Outline platelets.
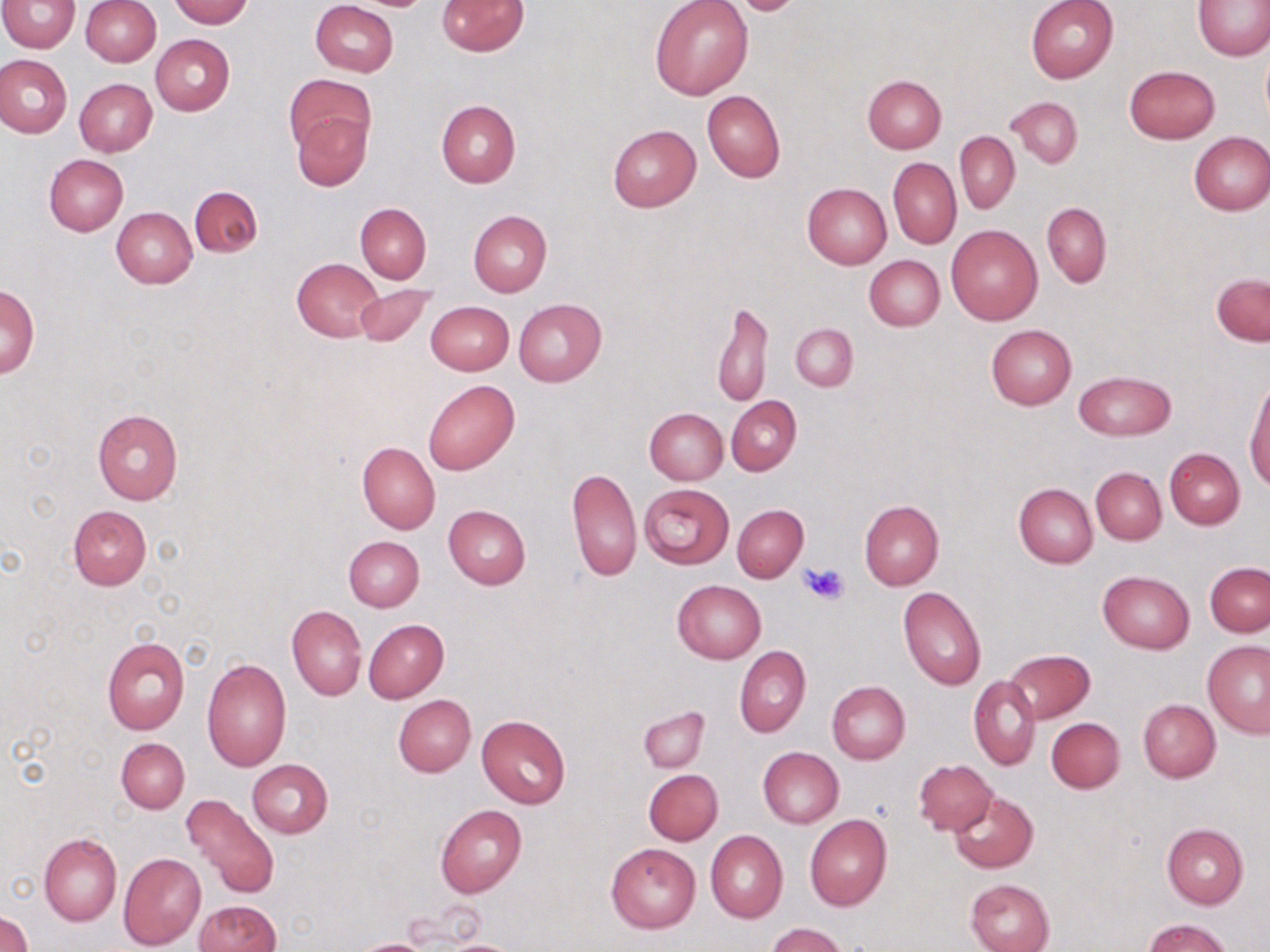

Approximate bounding boxes as [x1, y1, x2, y2] in pixels.
Platelets: [800, 561, 851, 605].

Summary:
  - Uninfected red blood cell locations: [168, 0, 252, 27], [310, 0, 399, 77], [721, 0, 807, 14], [1026, 0, 1120, 84], [1195, 0, 1270, 61], [1, 1, 80, 52], [81, 1, 161, 65], [437, 1, 528, 56], [649, 1, 753, 100], [151, 35, 235, 116], [1260, 44, 1270, 126], [0, 54, 72, 139], [1124, 65, 1219, 144], [285, 73, 375, 155], [862, 76, 947, 153], [74, 78, 157, 156], [701, 90, 785, 183], [1007, 96, 1084, 169], [436, 100, 520, 187], [293, 110, 371, 190], [607, 124, 701, 212], [955, 132, 1020, 213], [1188, 132, 1270, 216], [43, 154, 128, 235], [888, 158, 960, 248], [802, 183, 891, 268], [190, 185, 262, 256], [355, 202, 431, 283], [1042, 202, 1111, 287], [111, 207, 197, 289], [468, 209, 552, 296], [946, 224, 1042, 324], [864, 255, 945, 331], [292, 258, 383, 341], [1211, 274, 1269, 346], [1, 282, 38, 379], [353, 284, 435, 345], [514, 299, 606, 387], [425, 301, 514, 375], [712, 302, 773, 408], [790, 323, 858, 391], [986, 324, 1077, 409], [1074, 370, 1175, 440], [423, 379, 520, 475], [1246, 381, 1270, 491], [726, 396, 802, 475], [644, 408, 727, 485], [93, 410, 183, 504], [357, 442, 440, 534], [1165, 447, 1244, 529], [568, 467, 641, 583], [1091, 467, 1167, 544], [1014, 483, 1098, 568], [639, 484, 733, 569], [860, 499, 943, 590], [443, 504, 531, 588], [733, 504, 808, 582], [68, 505, 151, 590], [344, 535, 424, 612], [1205, 562, 1269, 636], [1098, 570, 1195, 654], [671, 580, 765, 664], [898, 586, 986, 692], [287, 606, 367, 700], [363, 620, 449, 703], [101, 636, 189, 734], [1201, 641, 1270, 737], [735, 646, 811, 738], [1004, 648, 1094, 723], [202, 658, 291, 772], [970, 676, 1041, 771], [827, 681, 910, 764], [393, 694, 475, 777], [1138, 699, 1220, 782], [639, 707, 709, 772], [477, 715, 570, 808], [1046, 718, 1125, 793], [117, 737, 189, 812], [758, 747, 844, 828], [247, 759, 333, 838], [914, 759, 997, 836], [644, 769, 724, 845], [949, 791, 1038, 873], [182, 793, 281, 901], [435, 805, 526, 898], [805, 813, 892, 911], [1161, 824, 1248, 909], [706, 830, 787, 923], [39, 834, 122, 926], [606, 843, 701, 933], [118, 852, 206, 950], [965, 878, 1056, 952], [192, 900, 280, 952], [0, 911, 33, 952], [1142, 918, 1233, 952], [767, 923, 847, 952], [351, 938, 436, 952]
  - Slide-level diagnosis: no evidence of blood parasites
  - Image size: 1270×952 pixels
  - Stain: May-Grünwald-Giemsa
  - Field of view: one of a larger specimen
  - Modality: light microscopy
  - Magnification: 1000x
  - Preparation: thin blood smear